Locate and identify every blood parasite.
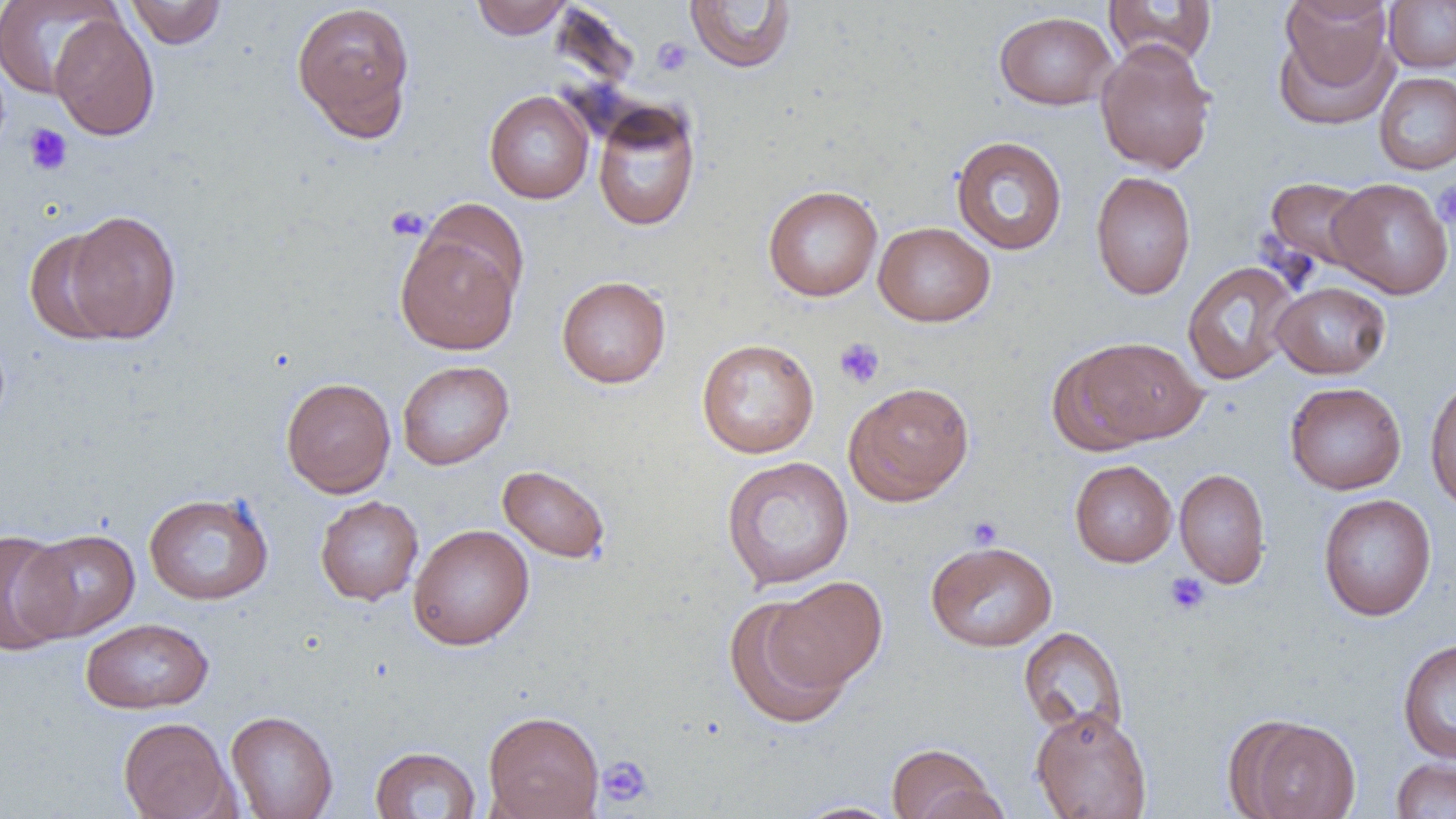
No blood parasites observed.

slide-level diagnosis = negative for blood parasites
preparation = thin blood film
magnification = 1000x
field of view = one of a larger specimen
image size = 1456×819 pixels
platelet locations = approximate bounding boxes as [x1, y1, x2, y2] in pixels: [651, 37, 693, 76], [23, 123, 73, 176], [1433, 181, 1456, 229], [385, 205, 429, 241], [834, 337, 885, 389], [967, 516, 1003, 549], [1164, 572, 1210, 616], [597, 755, 655, 808]
uninfected red blood cell locations = approximate bounding boxes as [x1, y1, x2, y2] in pixels: [0, 0, 121, 99], [125, 0, 226, 49], [471, 0, 573, 40], [1103, 0, 1217, 68], [291, 1, 416, 140], [684, 1, 797, 73], [1384, 1, 1456, 72], [1275, 9, 1395, 124], [994, 11, 1118, 110], [49, 13, 160, 141], [1095, 40, 1217, 175], [1374, 72, 1456, 175], [484, 90, 594, 204], [591, 100, 701, 232], [951, 135, 1068, 255], [1090, 171, 1195, 300], [1263, 177, 1375, 274], [1328, 178, 1454, 299], [762, 185, 883, 302], [61, 209, 182, 344], [873, 222, 995, 326], [395, 227, 522, 355], [23, 228, 125, 345], [1182, 261, 1299, 385], [557, 275, 671, 389], [1271, 281, 1392, 379], [1060, 335, 1207, 448], [696, 338, 820, 459], [397, 360, 514, 470], [1424, 375, 1456, 515], [281, 377, 396, 498], [1285, 381, 1406, 495], [844, 382, 975, 506], [721, 456, 854, 590], [1070, 460, 1177, 567], [497, 464, 611, 564], [1174, 468, 1271, 588], [143, 491, 274, 605], [1318, 493, 1437, 621], [315, 495, 424, 606], [408, 524, 534, 650], [0, 528, 76, 653], [19, 529, 140, 640], [926, 540, 1057, 652], [768, 575, 888, 693], [723, 594, 852, 728], [80, 617, 214, 714], [1018, 627, 1128, 740], [1397, 638, 1456, 763], [1031, 707, 1152, 819], [225, 710, 338, 819], [483, 710, 604, 819], [118, 716, 235, 819], [1232, 716, 1361, 819], [886, 743, 1003, 819], [369, 745, 482, 818], [1390, 758, 1456, 818], [793, 801, 904, 818]
modality = light microscopy